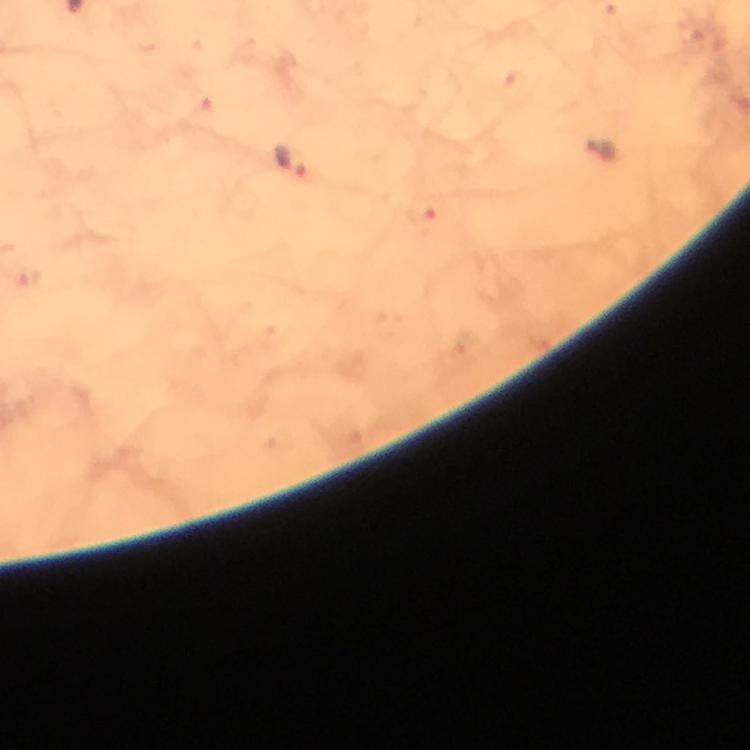
malaria parasite locations = approximate centers as (x, y) in pixels: (599, 148), (292, 162)
image size = 750×750 pixels
context = from a diagnostic examination for malaria
capture = smartphone photograph through a microscope
immersion oil = used
preparation = thick blood film
cropped from = a single field of view
stain = Giemsa
magnification = 100x